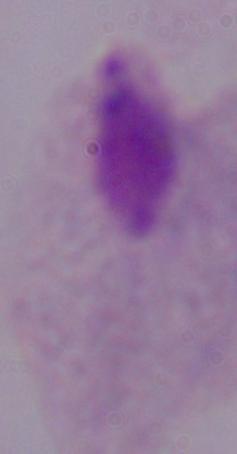
magnification = 1000x
identification = trichomonad
modality = photomicrograph